Outline platelets.
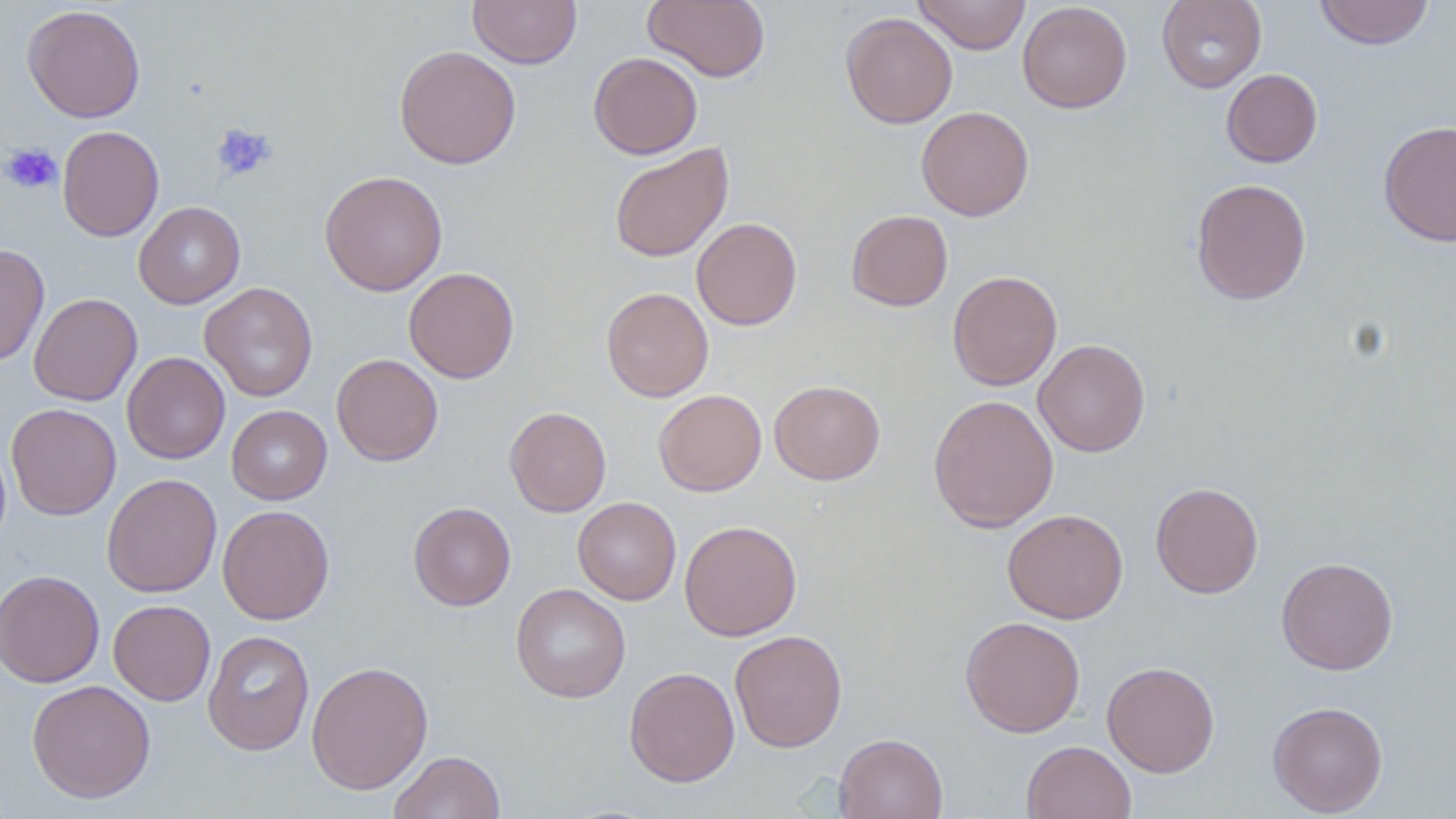
Approximate bounding boxes as (x1,y1)-(x2,y2) corner pairs in pixels.
Platelets: (211,123)-(277,181), (1,143)-(63,195).

Uninfected red blood cell locations: (468,0)-(581,68), (643,0)-(771,83), (913,0)-(1031,55), (1156,0)-(1267,93), (1314,0)-(1434,50), (1017,1)-(1132,113), (22,4)-(146,123), (841,12)-(958,129), (394,44)-(521,169), (588,52)-(703,159), (1221,68)-(1323,167), (916,105)-(1035,221), (1378,120)-(1456,247), (57,125)-(164,242), (609,143)-(733,262), (320,170)-(448,296), (1191,178)-(1312,305), (133,201)-(246,309), (846,209)-(953,311), (691,217)-(802,331), (0,243)-(49,367), (404,267)-(520,383), (948,270)-(1063,390), (200,282)-(318,402), (601,287)-(714,402), (29,293)-(142,406), (1033,339)-(1150,457), (122,352)-(230,464), (331,353)-(443,465), (769,380)-(885,485), (653,389)-(767,496), (928,394)-(1059,532), (6,403)-(121,520), (226,405)-(332,504), (505,406)-(612,517), (101,474)-(222,598), (1150,482)-(1263,598), (572,497)-(681,604), (408,502)-(516,610), (217,504)-(335,625), (1002,508)-(1128,624), (679,520)-(802,641), (1276,557)-(1398,675), (0,569)-(106,688), (511,583)-(631,703), (108,600)-(216,706), (960,615)-(1086,737), (203,630)-(315,756), (730,630)-(848,753), (306,660)-(433,795), (1102,661)-(1220,777), (624,666)-(739,787), (27,679)-(156,803), (1268,700)-(1388,816), (833,733)-(948,819), (1022,740)-(1136,819), (389,751)-(506,818). Slide-level diagnosis: no evidence of blood parasites. Thin blood film. Optical microscopy. Single field of view. 1000x magnification. Image is 1456×819 pixels. May-Grünwald-Giemsa stain.